Assess the morphology of the red blood cells.
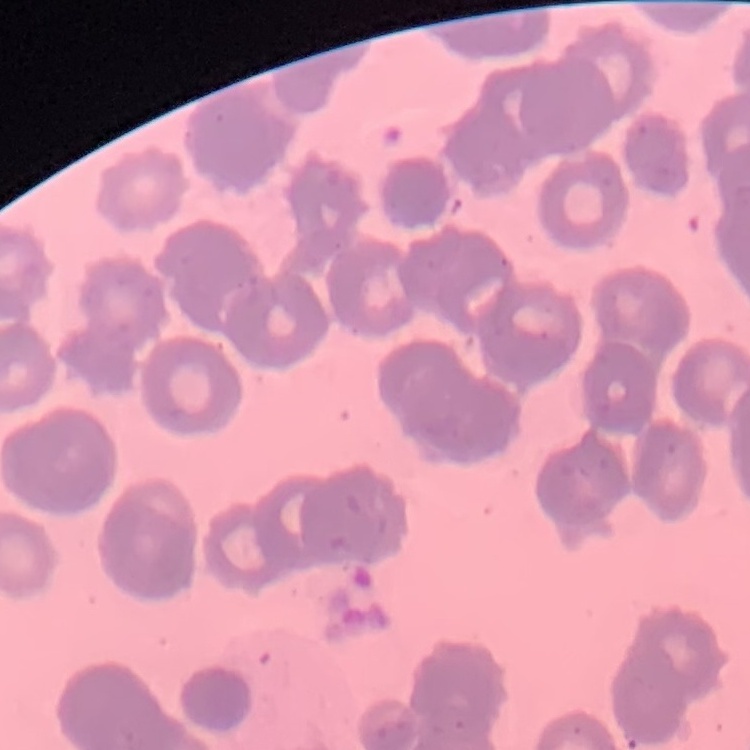

Rouleaux formation.

preparation = thin blood smear
stain = Field's or Giemsa
image type = square crop of a larger photomicrograph